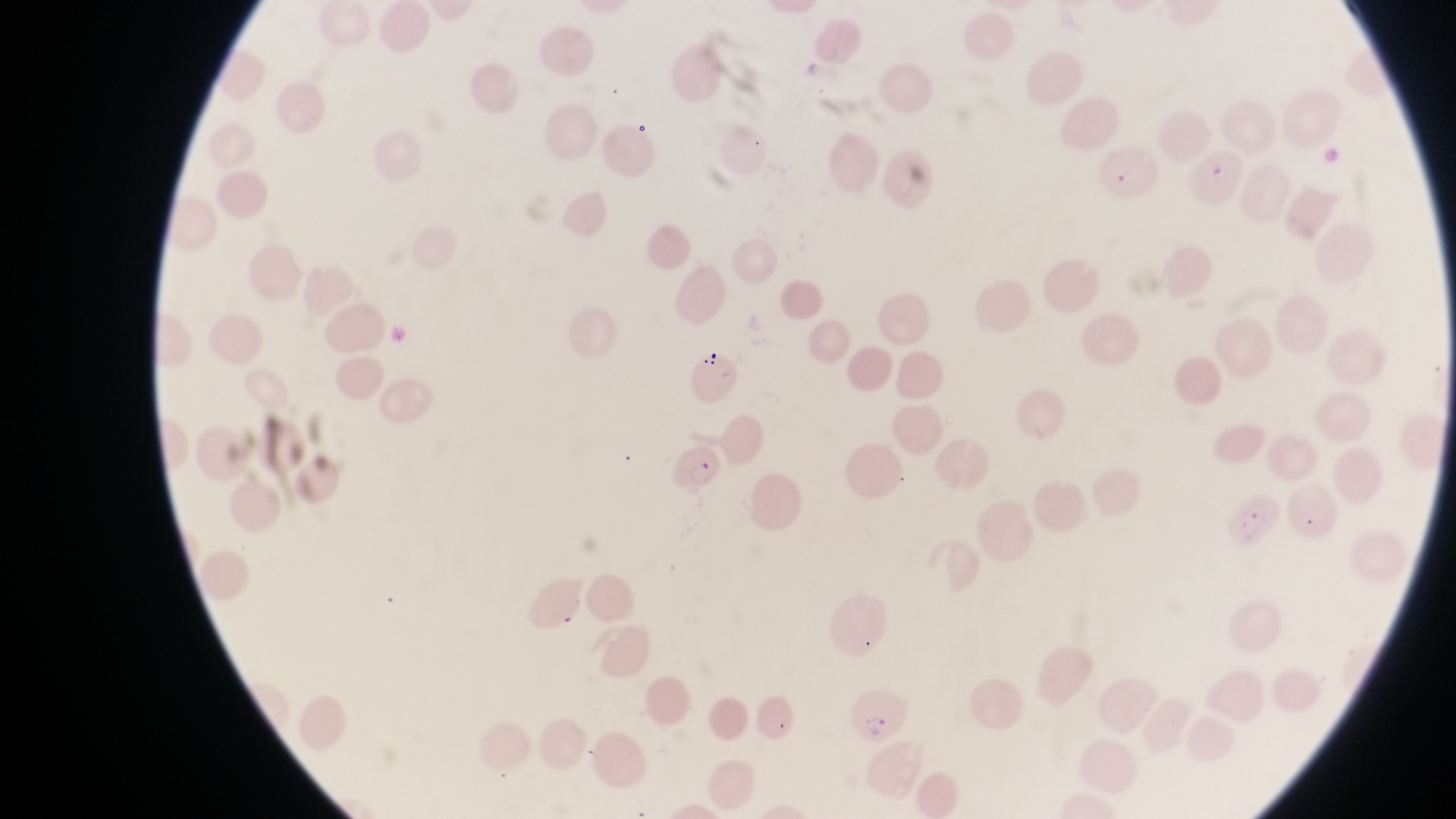

parasitised red blood cell locations = approximate bounding boxes as (left, top, right, bottom) in pixels: (1192, 140, 1245, 203), (1100, 146, 1171, 195), (666, 442, 727, 502), (849, 689, 908, 745)
capture = smartphone photograph through the eyepiece of an Olympus CX-23 microscope
preparation = thin blood film
image size = 1456×819 pixels
field of view = single
magnification = 1000x
country = Uganda